Locate and identify every blood parasite.
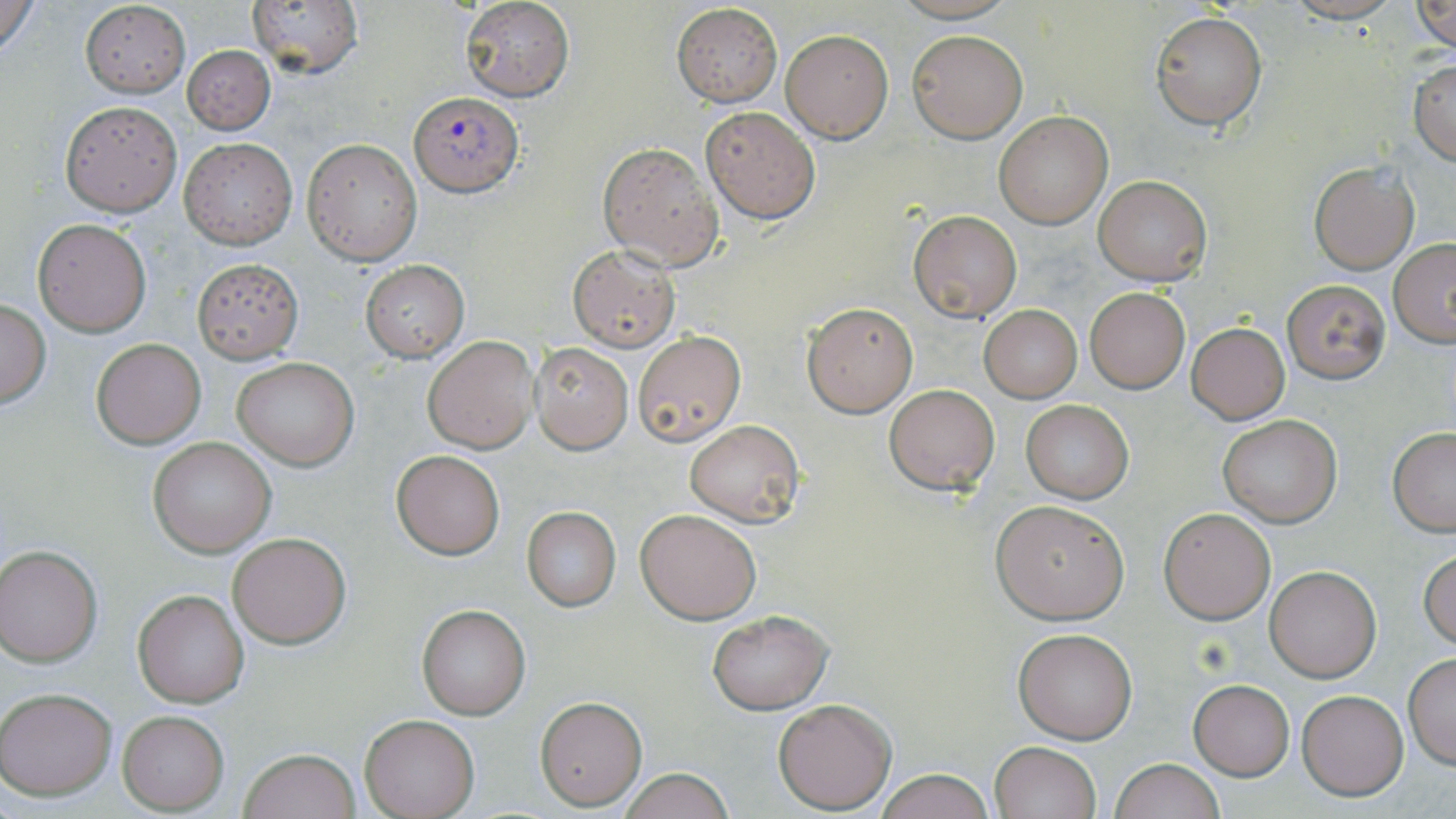

Approximate bounding boxes as (x1, y1, x2, y2) in pixels.
Plasmodium falciparum-infected red blood cells: (409, 92, 522, 196).
No Plasmodium ovale, Plasmodium malariae, Plasmodium vivax, Babesia divergens, or Trypanosoma brucei observed.

Summary:
  - Uninfected red blood cell locations: (0, 0, 42, 59), (246, 0, 363, 78), (459, 0, 574, 103), (1282, 0, 1405, 23), (1413, 0, 1456, 50), (80, 2, 189, 95), (671, 3, 782, 107), (1151, 10, 1266, 129), (779, 28, 893, 143), (907, 29, 1028, 142), (182, 44, 276, 135), (1410, 58, 1456, 164), (59, 100, 182, 216), (699, 105, 821, 223), (994, 111, 1113, 228), (178, 137, 297, 247), (301, 138, 422, 265), (597, 142, 725, 271), (1309, 163, 1420, 274), (1094, 175, 1211, 285), (908, 210, 1022, 319), (34, 220, 150, 335), (1389, 239, 1456, 345), (569, 246, 680, 352), (193, 258, 302, 362), (359, 259, 469, 361), (1282, 280, 1390, 384), (1084, 287, 1190, 393), (0, 299, 51, 407), (802, 302, 917, 416), (980, 307, 1082, 403), (1186, 323, 1290, 422), (632, 330, 745, 444), (423, 336, 537, 453), (92, 339, 205, 448), (531, 343, 633, 453), (232, 356, 359, 470), (883, 383, 1000, 495), (1020, 400, 1133, 502), (1216, 413, 1342, 528), (684, 420, 805, 528), (1388, 427, 1456, 534), (147, 437, 276, 557), (390, 449, 505, 559), (991, 498, 1131, 622), (521, 507, 620, 610), (1158, 507, 1276, 623), (635, 508, 763, 624), (228, 533, 352, 648), (0, 544, 103, 666), (1419, 549, 1456, 650), (1265, 565, 1380, 681), (132, 588, 248, 708), (417, 605, 530, 719), (706, 608, 832, 713), (1014, 627, 1137, 744), (1404, 654, 1456, 768), (1189, 680, 1293, 780), (1, 687, 118, 800), (1296, 688, 1409, 800), (534, 694, 647, 810), (773, 697, 897, 814), (116, 709, 230, 814), (360, 715, 481, 818), (990, 740, 1101, 819), (237, 748, 362, 819), (1110, 759, 1225, 819), (619, 768, 734, 819), (870, 768, 996, 819)
  - Slide-level diagnosis: Plasmodium falciparum
  - Magnification: 1000x
  - Modality: optical microscopy
  - Image size: 1456×819 pixels
  - Preparation: thin blood smear
  - Stain: May-Grünwald-Giemsa
  - Field of view: one of a larger specimen